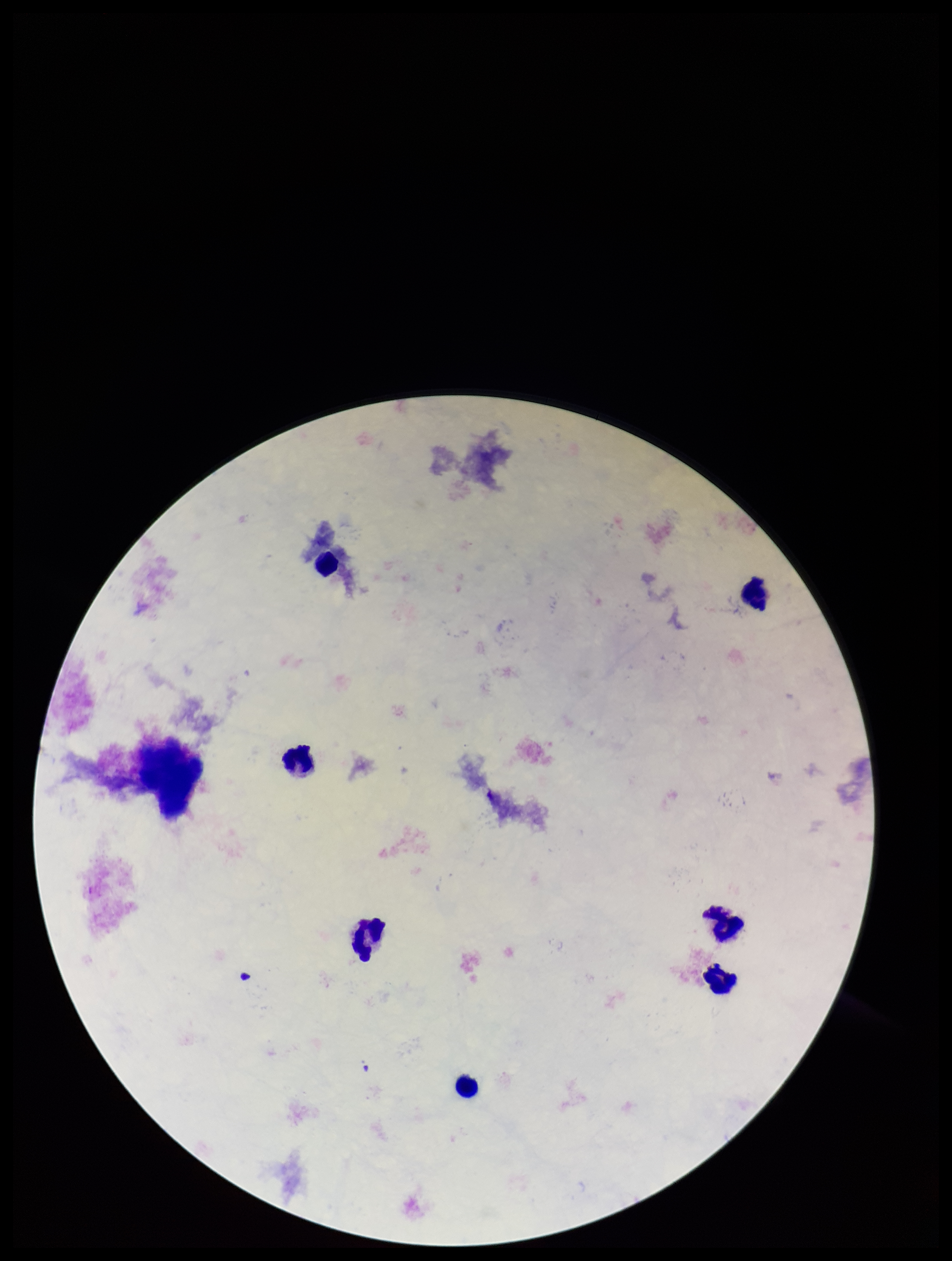

Plasmodium parasites = none detected
stain = Giemsa
preparation = thick smear
capture = smartphone photograph through the microscope eyepiece
leukocyte count = 7
patient malaria status = negative
image size = 952×1261 pixels
field of view = single
parasite count = 0